Classify this cell by malaria status.
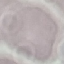
It is uninfected.

stain = Giemsa
image type = cell patch, automatically extracted from a larger field of view and resized to 64 × 64 pixels
preparation = thin blood film
capture = smartphone through the microscope eyepiece